Assess this cell for malaria.
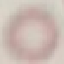
It is uninfected.

{
  "capture": "smartphone camera at the microscope eyepiece",
  "image_type": "cell patch, automatically extracted from a larger field of view and resized to 64 × 64 pixels",
  "preparation": "thin blood film",
  "stain": "Giemsa"
}